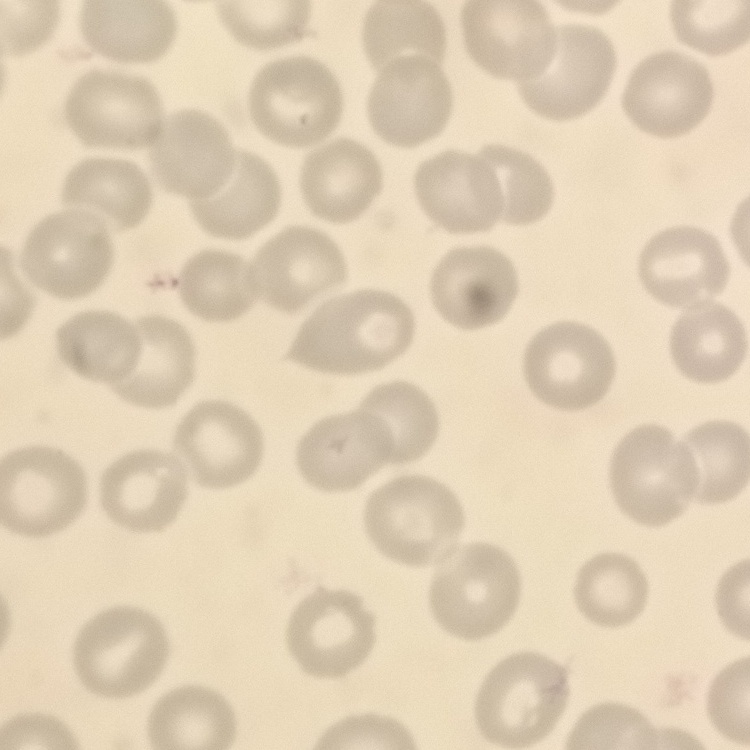

The erythrocytes show no rouleaux formation. Field's or Giemsa stain. Thin blood film. Square crop of a larger photomicrograph.